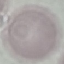
malaria_status: uninfected
stain: Giemsa
capture: smartphone camera at the microscope eyepiece
preparation: thin blood film
image_type: automatically extracted cell patch, resized to 64 × 64 pixels